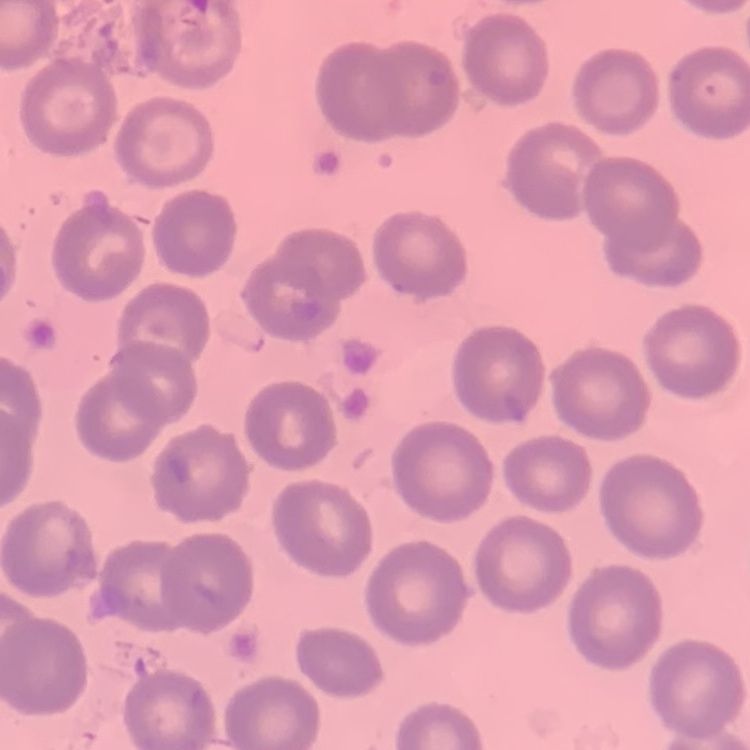
The erythrocytes exhibit no rouleaux formation. Square crop of a larger photomicrograph. Stained with either Field's or Giemsa. Thin blood smear.